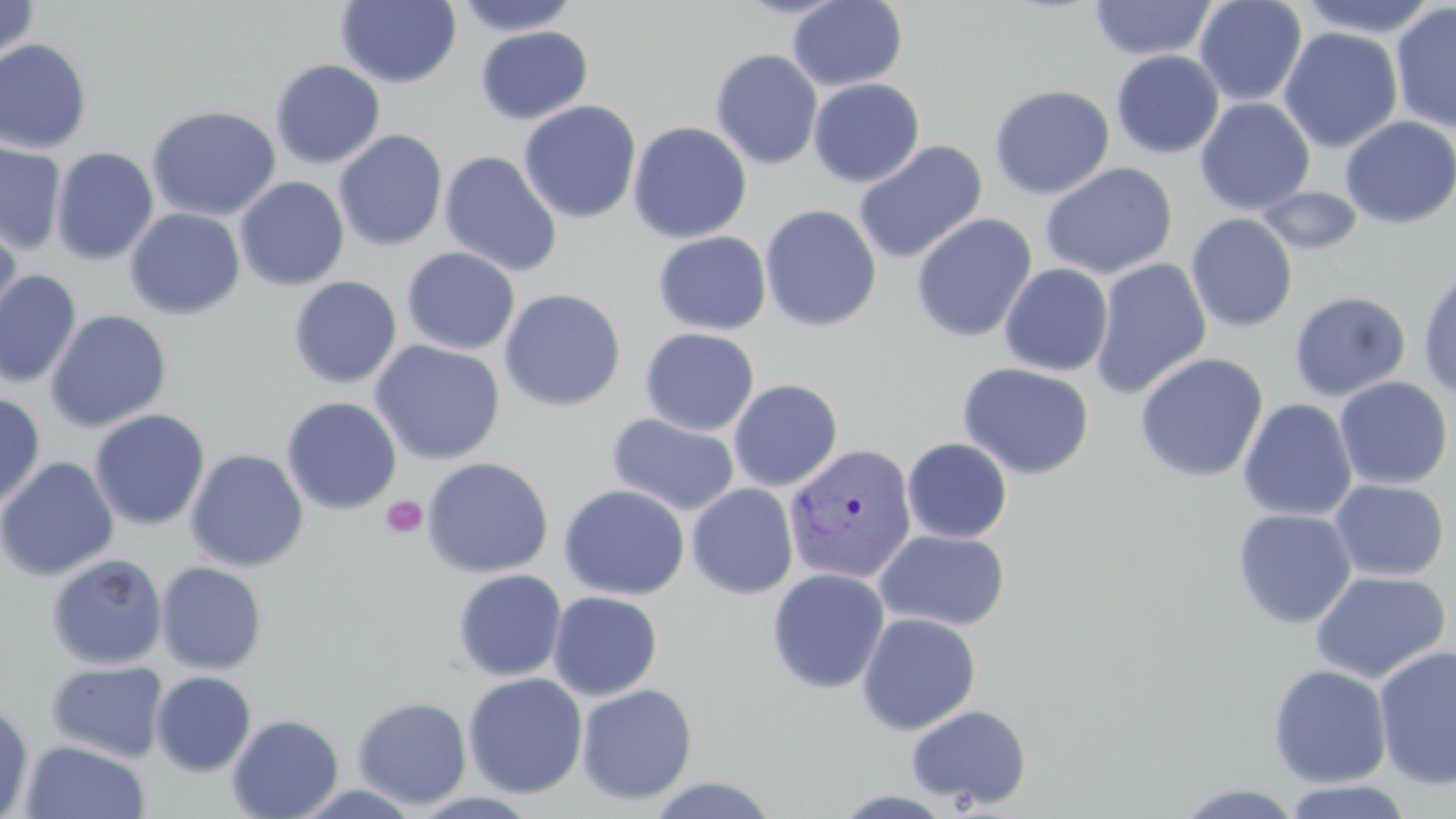
Approximate bounding boxes as (x1,y1)-(x2,y2) corner pairs in pixels. Plasmodium vivax-infected red blood cell locations: (783,443)-(916,584). Uninfected red blood cell locations: (0,0)-(39,63), (335,0)-(462,88), (452,0)-(582,36), (787,0)-(908,91), (1088,0)-(1218,62), (1194,0)-(1307,107), (1295,0)-(1442,38), (1391,2)-(1456,133), (474,27)-(593,124), (1279,27)-(1403,154), (0,39)-(93,155), (710,49)-(823,170), (1110,50)-(1225,159), (269,59)-(386,169), (808,78)-(925,187), (989,84)-(1115,200), (1194,97)-(1315,215), (518,100)-(641,224), (146,105)-(282,222), (1191,109)-(1302,314), (1339,116)-(1456,229), (628,122)-(752,243), (333,129)-(448,252), (852,140)-(987,264), (0,141)-(67,256), (51,146)-(159,266), (439,150)-(562,277), (1040,162)-(1178,280), (234,177)-(349,291), (1255,186)-(1364,255), (759,204)-(882,332), (125,208)-(245,320), (1186,213)-(1298,333), (911,214)-(1037,342), (0,218)-(23,337), (653,231)-(771,336), (401,247)-(520,355), (1089,257)-(1212,399), (999,263)-(1113,376), (1417,267)-(1456,401), (0,269)-(82,389), (288,275)-(402,389), (499,288)-(626,412), (1289,291)-(1412,401), (45,309)-(172,433), (640,327)-(760,436), (369,340)-(506,465), (1134,352)-(1268,483), (957,362)-(1095,481), (1334,377)-(1454,490), (728,379)-(843,492), (0,392)-(46,510), (281,396)-(402,515), (1237,398)-(1358,522), (89,409)-(210,531), (606,413)-(740,517), (902,438)-(1013,543), (185,449)-(309,573), (0,456)-(119,582), (421,456)-(554,578), (1329,479)-(1449,582), (558,484)-(690,600), (686,484)-(799,599), (1231,508)-(1357,629), (875,529)-(1011,631), (46,553)-(168,669), (155,561)-(268,674), (767,568)-(890,694), (452,569)-(567,682), (1310,570)-(1451,683), (548,591)-(663,701), (856,612)-(981,736), (1373,644)-(1456,789), (46,660)-(169,763), (1268,664)-(1393,788), (150,671)-(257,776), (463,672)-(588,798), (575,683)-(698,805), (352,696)-(472,809), (0,700)-(34,818), (906,704)-(1032,809), (227,713)-(344,819), (21,739)-(151,819), (646,776)-(780,818), (1280,779)-(1415,819), (1174,782)-(1305,819), (831,790)-(960,818). Platelet locations: (381,495)-(428,539). Slide-level diagnosis: Plasmodium vivax. Single field of view. Image is 1456×819 pixels. May-Grünwald-Giemsa stain. Optical microscopy. Thin blood film. 1000x magnification.